Classify this cell by malaria status.
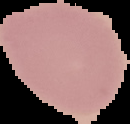
It is uninfected.

Summary:
  - Image type: segmented cell region with the area outside set to black
  - Preparation: thin blood film
  - Image size: 130×124 pixels